Name the parasite shown.
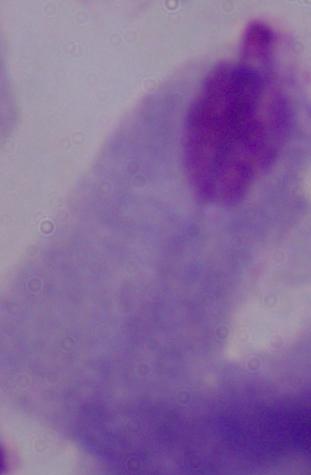

A trichomonad.

Photomicrograph. 1000x magnification.